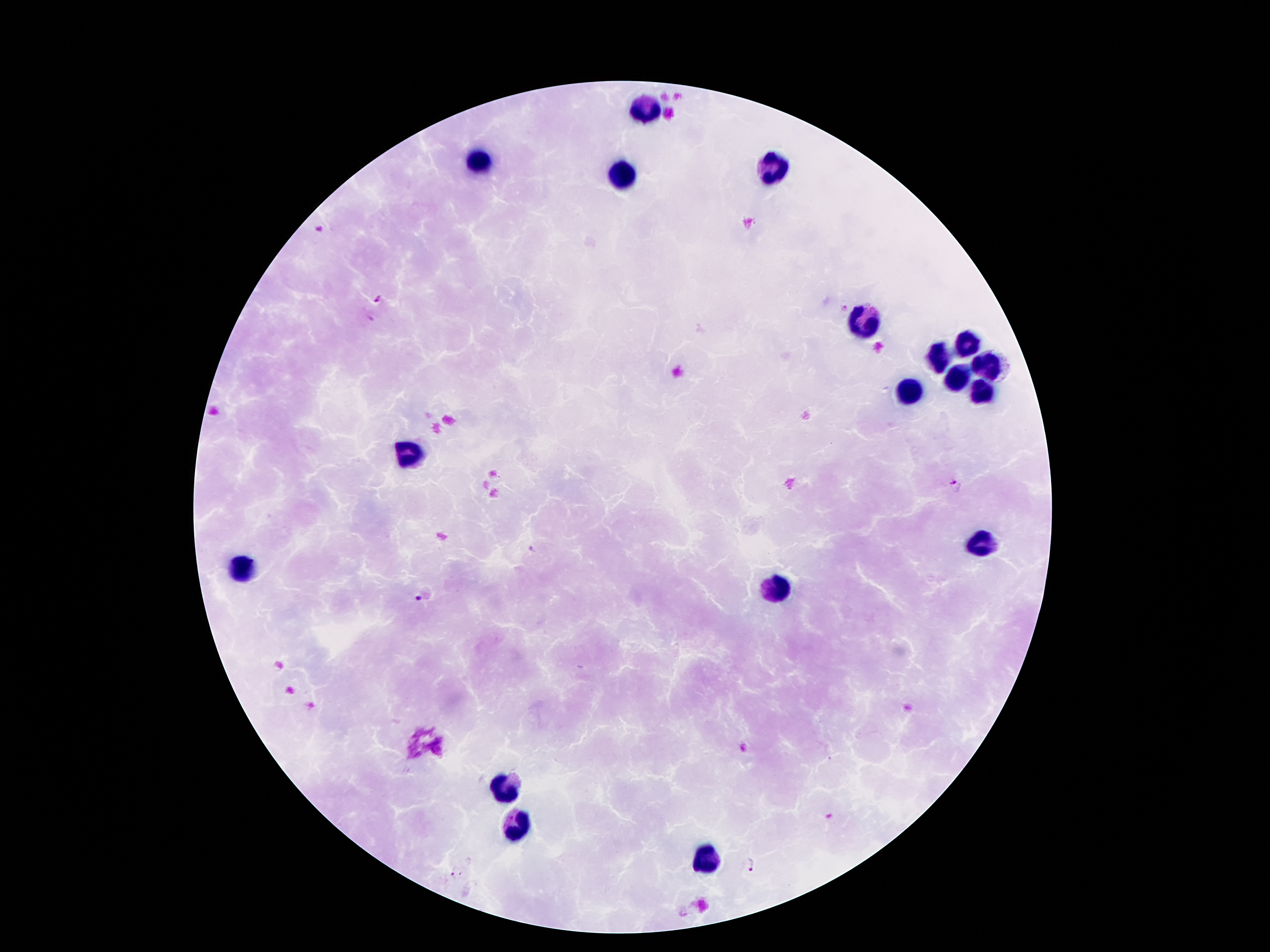 Approximate object centers, in pixels from the top-left corner. Leukocyte locations: (x=645, y=109), (x=479, y=163), (x=771, y=167), (x=621, y=175), (x=867, y=319), (x=965, y=343), (x=939, y=357), (x=985, y=365), (x=959, y=379), (x=911, y=393), (x=979, y=393), (x=407, y=455), (x=975, y=545), (x=239, y=563), (x=777, y=589), (x=505, y=787), (x=517, y=827), (x=713, y=859). Plasmodium parasite locations: (x=320, y=229), (x=379, y=300), (x=955, y=486), (x=533, y=550), (x=426, y=595), (x=751, y=865), (x=456, y=874). 100x magnification. One field from this slide. Thick peripheral-blood smear. Photographed through the microscope eyepiece with a smartphone camera. Patient malaria status: positive for Plasmodium falciparum. Image is 1270×952 pixels. Giemsa stain.